Classify this cell by malaria status.
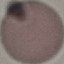

Uninfected.

image_type: cell patch, automatically extracted from a larger field of view and resized to 64 × 64 pixels
preparation: thin blood smear
capture: smartphone through the microscope eyepiece
stain: Giemsa